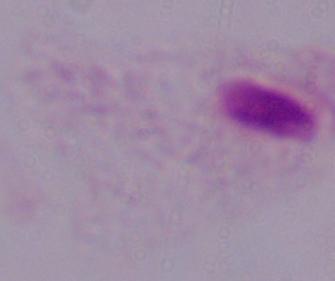
modality = photomicrograph
identification = trichomonad
magnification = 1000x